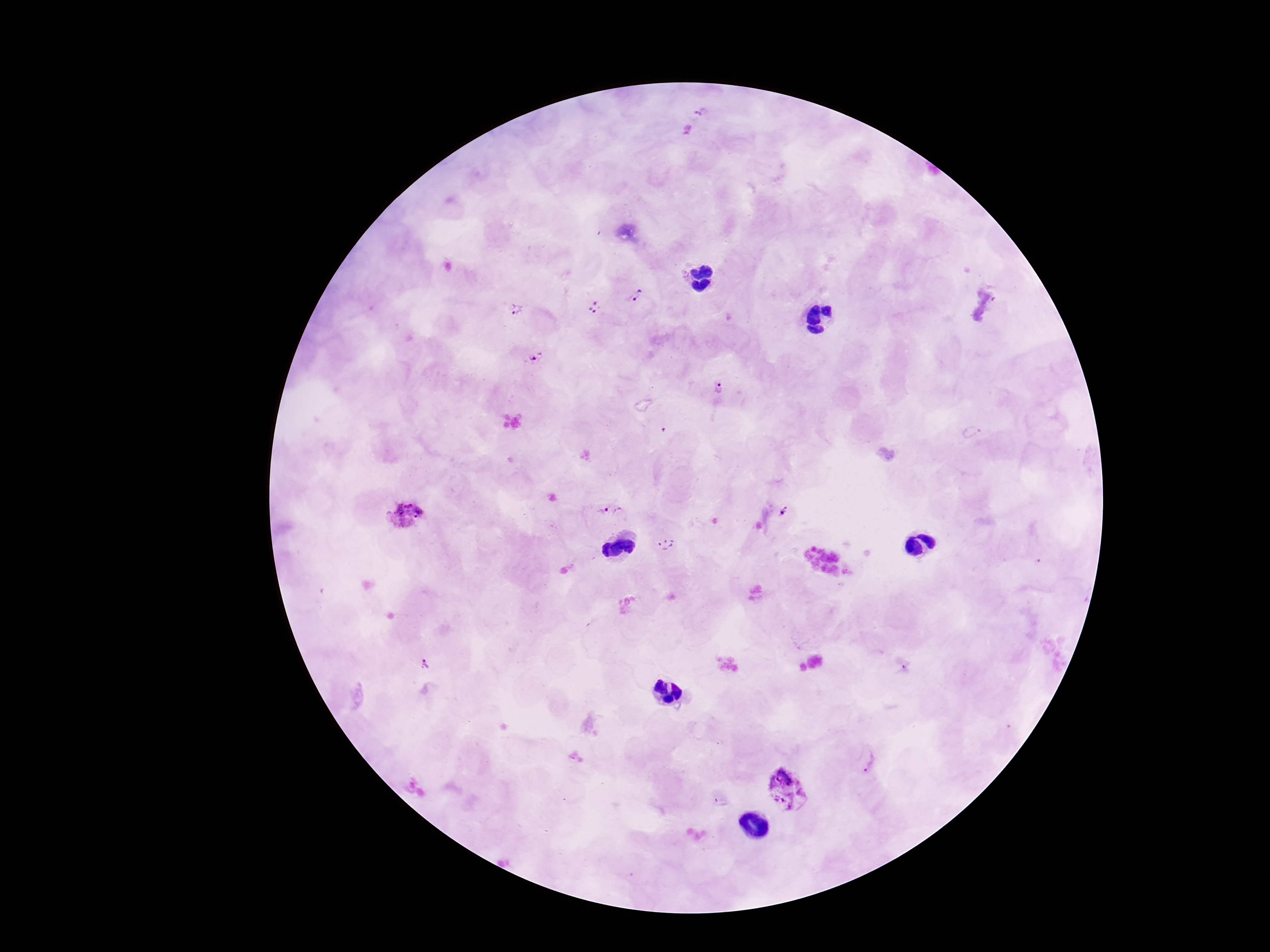

Approximate centers as [x, y] in pixels.
Summary:
  - Plasmodium parasite locations: [696, 112], [637, 296], [594, 304], [519, 309], [533, 357], [716, 387], [970, 432], [610, 508], [786, 513], [404, 515], [666, 543], [426, 664], [867, 759], [786, 788], [719, 803]
  - Stain: Giemsa
  - Image size: 1270×952 pixels
  - Patient malaria status: positive
  - Field of view: one from this slide
  - Preparation: thick blood film
  - Capture: smartphone camera through the microscope eyepiece
  - Magnification: 100x